Classify this cell by malaria status.
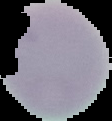
It is uninfected.

Summary:
  - Preparation: thin blood smear
  - Image type: segmented cell region on a black background
  - Image size: 112×121 pixels